Locate every blood parasite and identify its species.
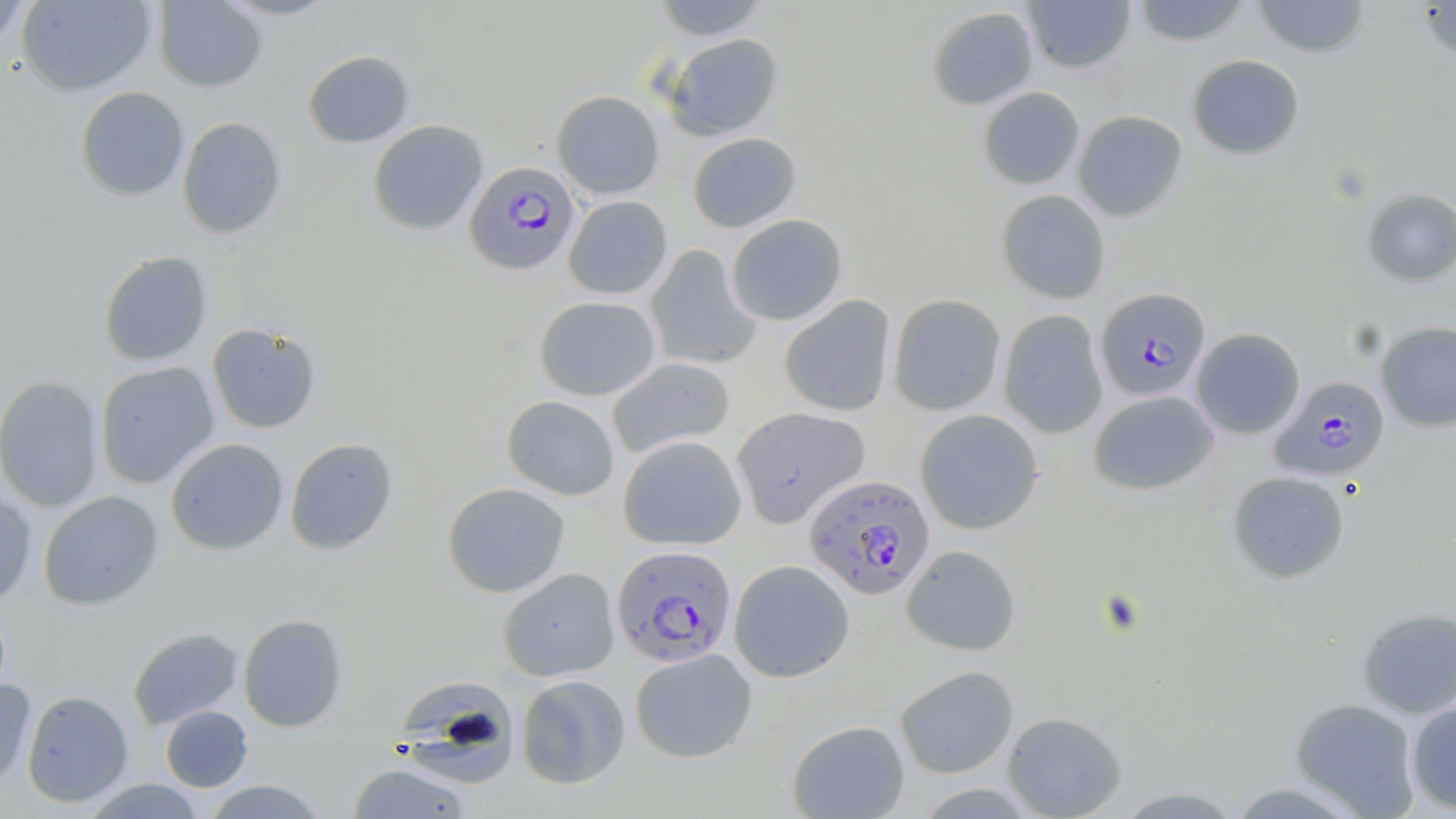
Approximate bounding boxes as [x1, y1, x2, y2] in pixels.
Plasmodium falciparum-infected red blood cells: [464, 160, 580, 276], [1095, 287, 1211, 401], [1270, 376, 1390, 481], [803, 474, 935, 600], [611, 545, 737, 668].
No Plasmodium ovale, Plasmodium malariae, Plasmodium vivax, Babesia divergens, or Trypanosoma brucei observed.

Uninfected red blood cell locations: [16, 0, 156, 96], [216, 0, 342, 21], [651, 0, 770, 41], [1130, 0, 1253, 46], [1252, 0, 1371, 58], [1415, 0, 1456, 61], [153, 1, 267, 92], [1022, 1, 1136, 75], [0, 2, 32, 52], [927, 5, 1038, 110], [664, 32, 784, 141], [302, 50, 415, 148], [1187, 54, 1305, 160], [75, 86, 189, 201], [977, 86, 1085, 190], [552, 90, 664, 199], [1073, 110, 1187, 220], [176, 117, 287, 239], [368, 119, 488, 235], [687, 132, 801, 233], [1360, 188, 1456, 286], [996, 189, 1111, 304], [563, 195, 673, 299], [725, 213, 847, 325], [645, 245, 761, 371], [98, 251, 212, 366], [888, 294, 1006, 415], [779, 295, 896, 416], [534, 296, 660, 400], [999, 309, 1108, 438], [207, 321, 322, 434], [1375, 321, 1456, 432], [1191, 327, 1306, 439], [607, 356, 735, 458], [95, 361, 219, 489], [0, 375, 104, 512], [1089, 390, 1218, 495], [501, 395, 620, 500], [731, 406, 870, 529], [915, 409, 1044, 535], [618, 435, 746, 550], [284, 437, 398, 556], [165, 438, 288, 555], [1228, 470, 1350, 583], [441, 482, 570, 597], [0, 483, 37, 609], [38, 491, 163, 610], [901, 544, 1021, 656], [729, 559, 855, 683], [498, 568, 620, 681], [1357, 607, 1456, 719], [238, 613, 348, 732], [128, 627, 244, 730], [629, 648, 758, 763], [894, 665, 1019, 779], [516, 674, 631, 788], [0, 679, 36, 788], [402, 679, 520, 793], [21, 690, 133, 807], [1290, 698, 1422, 817], [1406, 699, 1456, 813], [160, 705, 253, 791], [1002, 710, 1128, 818], [787, 719, 910, 818], [347, 761, 472, 818], [81, 778, 206, 818], [201, 779, 329, 818], [1223, 780, 1373, 818], [1112, 786, 1245, 818]. Slide-level diagnosis: Plasmodium falciparum. Light microscopy. May-Grünwald-Giemsa-stained preparation. 1000x magnification. One field of a larger specimen. Image is 1456×819 pixels. Thin blood smear.